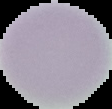

From a thin blood film. Image is 112×109 pixels. Result: no malaria parasites seen. Cell region segmented out of the field of view; the surrounding area is masked to black.